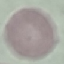

Summary:
  - Result: no malaria parasites seen
  - Stain: Giemsa
  - Image type: automatically extracted cell patch, resized to 64 × 64 pixels
  - Capture: smartphone through the microscope eyepiece
  - Preparation: thin blood film